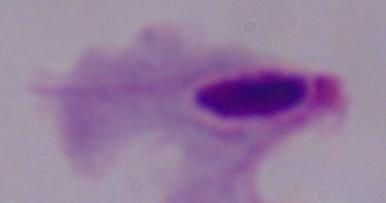 Captured at 1000x magnification. Micrograph. A trichomonad is seen.